Locate and identify every blood parasite.
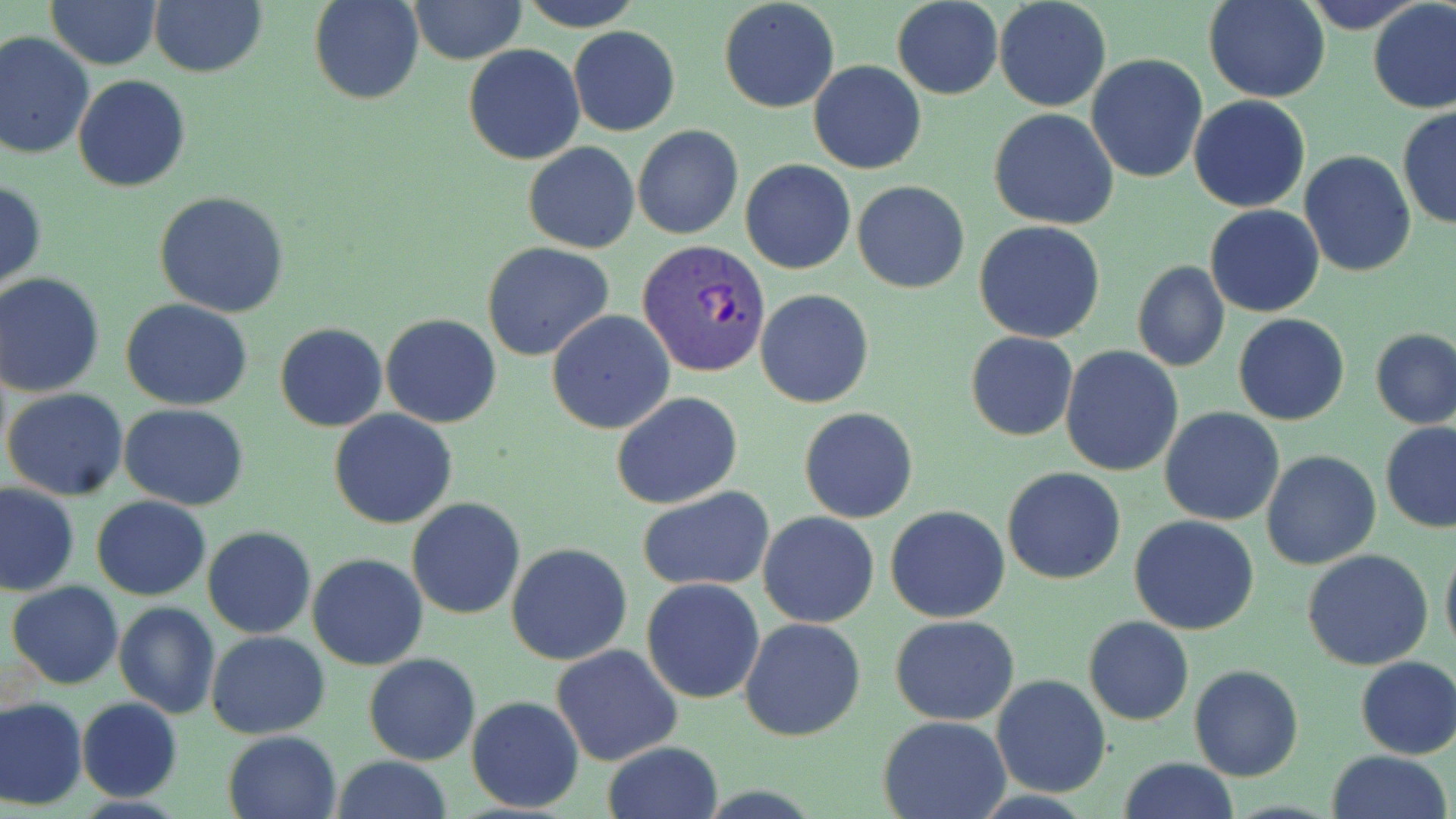
Approximate bounding boxes as named x1/y1/x2/y2 corners in pixels.
Plasmodium vivax-infected red blood cells: (x1=636, y1=239, x2=771, y2=378).
No Plasmodium falciparum, Plasmodium ovale, Plasmodium malariae, Babesia divergens, or Trypanosoma brucei observed.

Summary:
  - Uninfected red blood cell locations: (x1=311, y1=0, x2=423, y2=104), (x1=520, y1=0, x2=643, y2=31), (x1=718, y1=0, x2=840, y2=114), (x1=993, y1=0, x2=1111, y2=113), (x1=1203, y1=0, x2=1330, y2=102), (x1=1300, y1=0, x2=1425, y2=30), (x1=48, y1=1, x2=161, y2=70), (x1=409, y1=1, x2=527, y2=65), (x1=893, y1=1, x2=1003, y2=99), (x1=1368, y1=1, x2=1456, y2=114), (x1=150, y1=2, x2=266, y2=77), (x1=569, y1=26, x2=680, y2=136), (x1=0, y1=31, x2=95, y2=159), (x1=462, y1=44, x2=585, y2=165), (x1=1086, y1=54, x2=1207, y2=183), (x1=809, y1=60, x2=926, y2=174), (x1=73, y1=75, x2=191, y2=191), (x1=1188, y1=95, x2=1310, y2=213), (x1=1397, y1=107, x2=1455, y2=230), (x1=989, y1=109, x2=1118, y2=230), (x1=632, y1=124, x2=743, y2=240), (x1=524, y1=142, x2=639, y2=253), (x1=1298, y1=151, x2=1416, y2=277), (x1=740, y1=158, x2=855, y2=275), (x1=0, y1=179, x2=46, y2=295), (x1=852, y1=181, x2=970, y2=293), (x1=155, y1=191, x2=290, y2=317), (x1=1206, y1=204, x2=1324, y2=317), (x1=973, y1=220, x2=1106, y2=344), (x1=480, y1=241, x2=614, y2=361), (x1=1131, y1=260, x2=1230, y2=373), (x1=0, y1=274, x2=104, y2=396), (x1=756, y1=288, x2=874, y2=408), (x1=121, y1=299, x2=254, y2=411), (x1=547, y1=310, x2=676, y2=434), (x1=381, y1=313, x2=502, y2=427), (x1=1232, y1=313, x2=1349, y2=426), (x1=275, y1=323, x2=387, y2=432), (x1=1370, y1=329, x2=1455, y2=431), (x1=966, y1=332, x2=1077, y2=441), (x1=1060, y1=347, x2=1184, y2=477), (x1=3, y1=389, x2=128, y2=498), (x1=611, y1=391, x2=743, y2=509), (x1=120, y1=404, x2=250, y2=509), (x1=1159, y1=406, x2=1285, y2=527), (x1=799, y1=407, x2=918, y2=524), (x1=329, y1=410, x2=458, y2=529), (x1=1380, y1=421, x2=1456, y2=532), (x1=1261, y1=450, x2=1380, y2=569), (x1=1002, y1=466, x2=1126, y2=584), (x1=0, y1=483, x2=81, y2=597), (x1=4, y1=486, x2=95, y2=688), (x1=637, y1=488, x2=774, y2=591), (x1=91, y1=495, x2=211, y2=601), (x1=407, y1=498, x2=526, y2=620), (x1=885, y1=505, x2=1011, y2=623), (x1=757, y1=511, x2=881, y2=628), (x1=1129, y1=516, x2=1260, y2=636), (x1=203, y1=527, x2=316, y2=639), (x1=1440, y1=541, x2=1456, y2=659), (x1=506, y1=542, x2=633, y2=666), (x1=1302, y1=548, x2=1434, y2=671), (x1=307, y1=554, x2=427, y2=671), (x1=641, y1=578, x2=765, y2=703), (x1=7, y1=581, x2=124, y2=689), (x1=113, y1=601, x2=221, y2=720), (x1=889, y1=615, x2=1020, y2=726), (x1=1083, y1=616, x2=1194, y2=726), (x1=739, y1=617, x2=867, y2=742), (x1=206, y1=631, x2=330, y2=738), (x1=551, y1=644, x2=683, y2=767), (x1=364, y1=654, x2=481, y2=765), (x1=1355, y1=656, x2=1456, y2=759), (x1=1189, y1=665, x2=1303, y2=782), (x1=991, y1=675, x2=1111, y2=796), (x1=467, y1=695, x2=585, y2=814), (x1=0, y1=696, x2=87, y2=809), (x1=77, y1=697, x2=183, y2=803), (x1=878, y1=715, x2=1011, y2=819), (x1=223, y1=730, x2=341, y2=819), (x1=601, y1=741, x2=725, y2=819), (x1=1324, y1=750, x2=1454, y2=819), (x1=330, y1=757, x2=454, y2=818), (x1=1118, y1=757, x2=1239, y2=818)
  - Slide-level diagnosis: Plasmodium vivax
  - Stain: May-Grünwald-Giemsa
  - Magnification: 1000x
  - Preparation: thin blood film
  - Image size: 1456×819 pixels
  - Field of view: single
  - Modality: optical microscopy